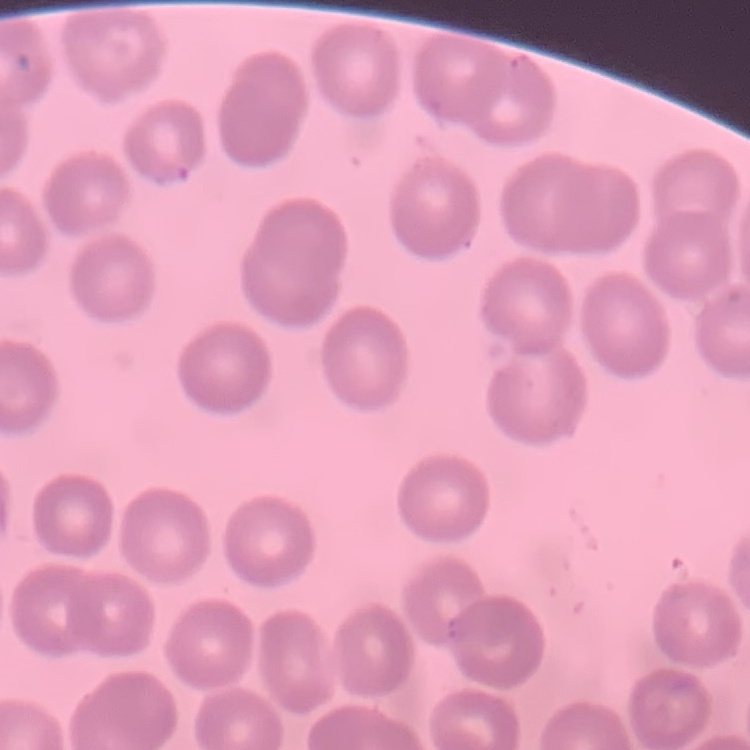

The erythrocytes show no rouleaux formation. Thin peripheral smear. Field's or Giemsa stain. One tile cut from a larger photomicrograph.